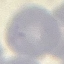
{
  "result": "negative for malaria parasites",
  "preparation": "thin blood smear",
  "image_type": "automatically extracted cell patch, resized to 64 × 64 pixels",
  "stain": "Giemsa",
  "capture": "smartphone camera at the microscope eyepiece"
}